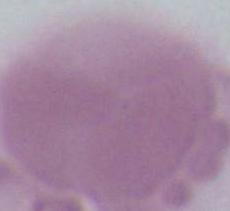

Photomicrograph. 1000x magnification. A red blood cell is shown.